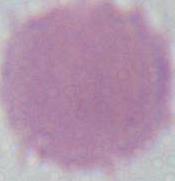

{
  "magnification": "1000x",
  "identification": "red blood cell",
  "modality": "photomicrograph"
}